Report the malaria status of this cell.
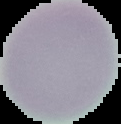

It is uninfected.

From a thin blood smear. Cell region segmented out of the field of view; the surrounding area is masked to black. Image is 121×124 pixels.